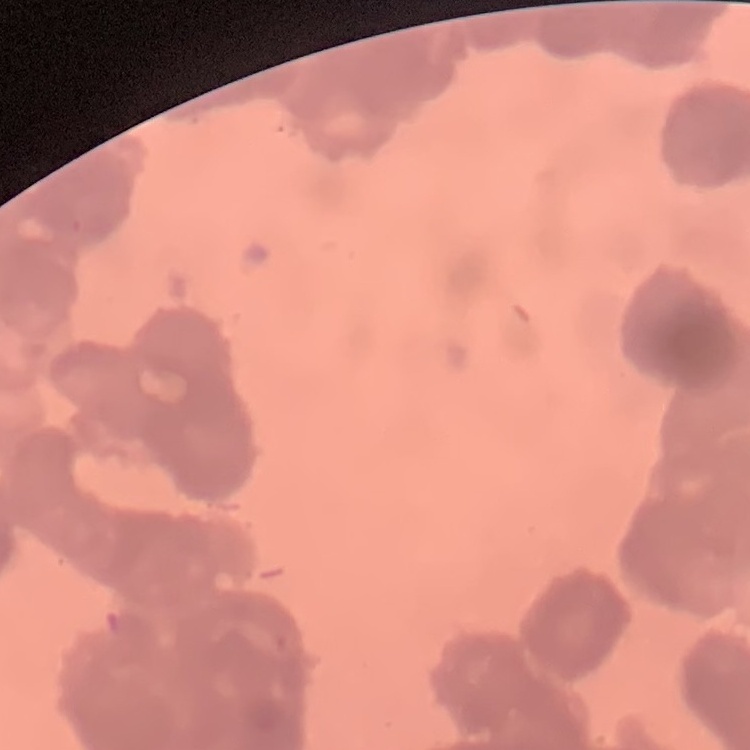 The red blood cells show rouleaux formation. Thin blood film. One tile cut from a larger photomicrograph. Field's or Giemsa stain.